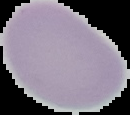

Summary:
  - Result: no Plasmodium parasites seen
  - Image size: 130×115 pixels
  - Image type: cell region segmented out of the field of view; surrounding area masked to black
  - Preparation: thin blood film